Report the malaria status of this cell.
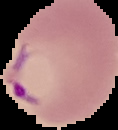
Parasitized.

From a thin blood smear. The area outside the segmented cell region is set to black. Image is 118×130 pixels.